Assess this cell for malaria.
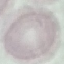

It is uninfected.

preparation = thin blood film
image type = automatically extracted cell patch, resized to 64 × 64 pixels
capture = smartphone camera at the microscope eyepiece
stain = Giemsa